Report the malaria status of this cell.
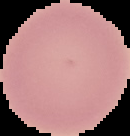
Uninfected.

Summary:
  - Image size: 130×136 pixels
  - Image type: segmented cell region on a black background
  - Preparation: thin blood film